Identify the parasite.
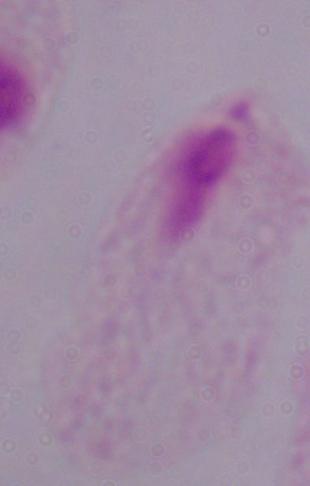

This is a trichomonad.

modality: micrograph
magnification: 1000x